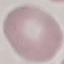
{
  "malaria_status": "uninfected",
  "preparation": "thin smear",
  "stain": "Giemsa",
  "capture": "smartphone camera at the microscope eyepiece",
  "image_type": "automatically extracted cell patch, resized to 64 × 64 pixels"
}